Classify this cell by malaria status.
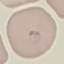

It is parasitized.

{
  "capture": "smartphone through the microscope eyepiece",
  "stain": "Giemsa",
  "preparation": "thin blood film",
  "image_type": "automatically extracted cell patch, resized to 64 × 64 pixels"
}